Outline each blood parasite and name the species.
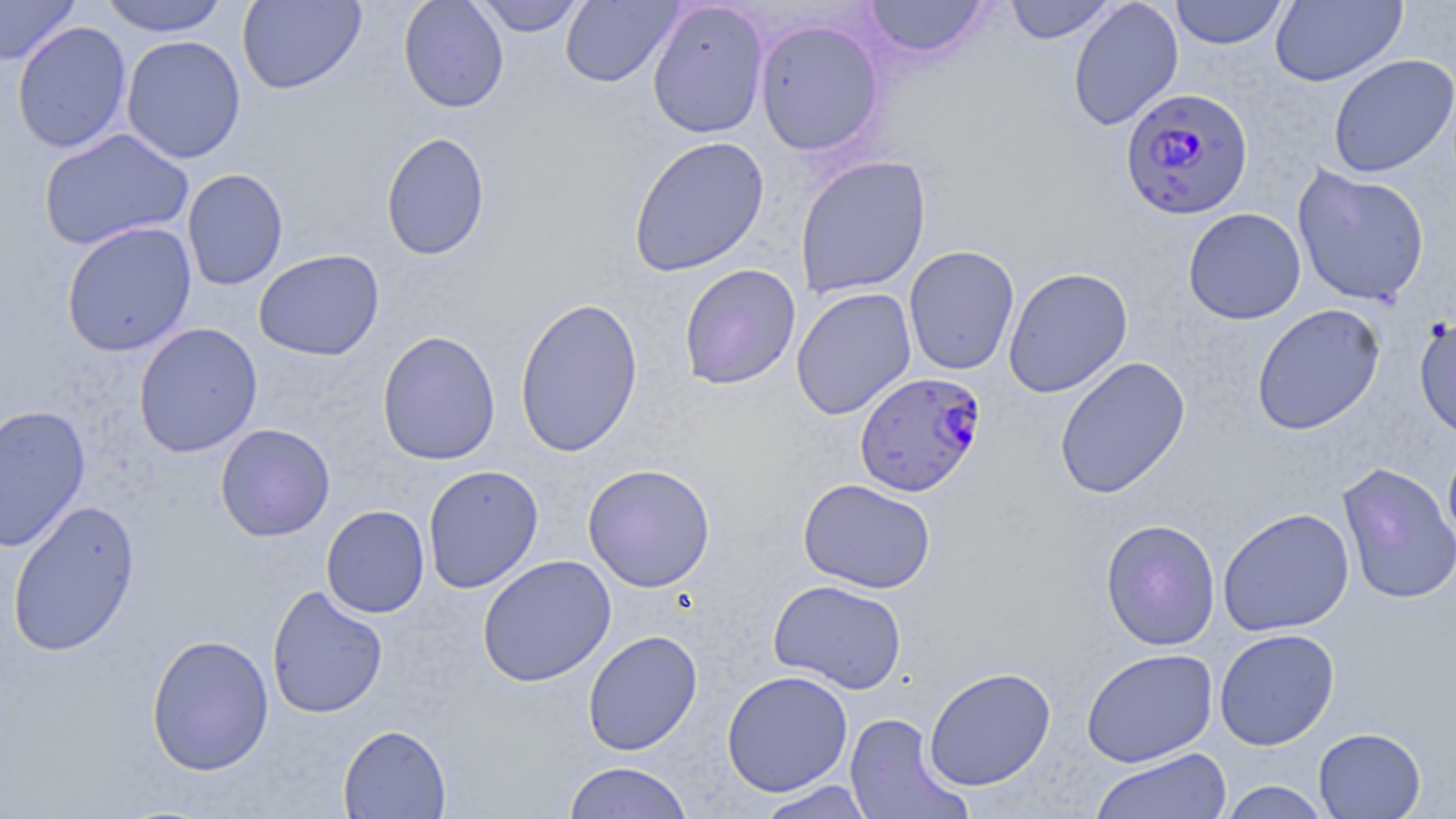

Approximate bounding boxes as (x1,y1)-(x2,y2) corner pairs in pixels.
Plasmodium falciparum-infected red blood cells: (1120,87)-(1254,220), (854,371)-(985,497).
No Plasmodium ovale, Plasmodium malariae, Plasmodium vivax, Babesia divergens, or Trypanosoma brucei observed.

Uninfected red blood cell locations: (0,0)-(79,66), (99,0)-(230,37), (237,0)-(366,94), (398,0)-(509,112), (471,0)-(588,37), (560,0)-(682,87), (863,0)-(989,61), (1003,0)-(1119,45), (1067,0)-(1184,132), (1169,0)-(1290,49), (1270,0)-(1407,86), (647,1)-(770,139), (754,19)-(886,156), (12,21)-(132,154), (121,35)-(246,163), (1328,54)-(1456,178), (39,128)-(194,251), (381,131)-(491,260), (627,135)-(770,277), (795,155)-(932,299), (1292,165)-(1430,307), (182,168)-(288,290), (1183,208)-(1306,324), (61,221)-(197,357), (903,245)-(1020,376), (253,249)-(385,361), (679,264)-(801,390), (1003,266)-(1133,398), (791,287)-(917,420), (514,296)-(643,458), (1251,304)-(1385,435), (1414,314)-(1456,442), (133,322)-(263,458), (377,330)-(501,466), (1054,356)-(1191,499), (0,404)-(91,552), (215,423)-(335,541), (1442,438)-(1456,553), (1337,462)-(1456,605), (582,463)-(716,592), (423,464)-(544,594), (798,478)-(936,593), (7,499)-(141,657), (321,505)-(430,618), (1217,507)-(1355,637), (1100,518)-(1221,651), (477,555)-(616,687), (768,579)-(907,694), (266,585)-(388,718), (1214,628)-(1340,750), (583,629)-(703,756), (146,633)-(274,776), (1081,648)-(1218,767), (924,666)-(1056,790), (721,670)-(853,797), (845,712)-(970,819), (338,724)-(451,818), (1313,727)-(1426,818), (1090,747)-(1231,819), (563,761)-(694,819), (754,780)-(878,818), (1217,781)-(1331,818). Slide-level diagnosis: Plasmodium falciparum. Thin blood smear. Light microscopy. One field of a larger specimen. Image is 1456×819 pixels. Captured at 1000x magnification. May-Grünwald-Giemsa-stained preparation.